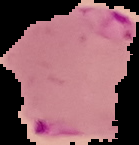 Malaria status: parasitized. From a thin blood film. Image is 139×145 pixels. Segmented cell region on a black background.